Outline platelets.
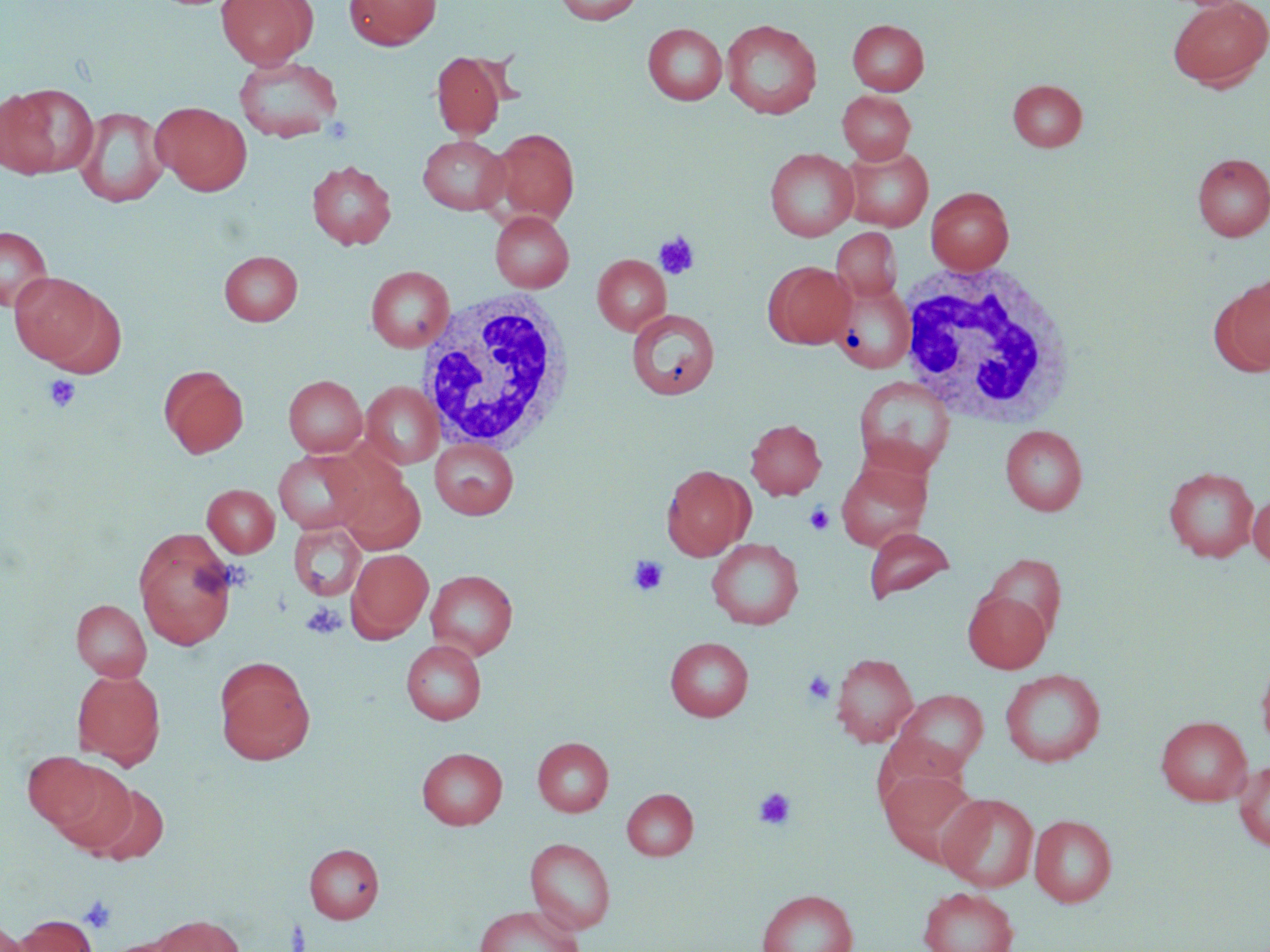

Approximate bounding boxes as [x1, y1, x2, y2] in pixels.
Platelets: [654, 231, 699, 280], [43, 374, 81, 412], [804, 503, 835, 535], [628, 555, 669, 596], [300, 602, 346, 639], [803, 671, 836, 705], [754, 787, 797, 830], [78, 894, 117, 933].

slide-level diagnosis = no evidence of blood parasites
magnification = 1000x
image size = 1270×952 pixels
stain = May-Grünwald-Giemsa
preparation = thin blood film
white blood cell locations = approximate bounding boxes as [x1, y1, x2, y2] in pixels: [894, 262, 1078, 428], [414, 288, 576, 454]
uninfected red blood cell locations = approximate bounding boxes as [x1, y1, x2, y2] in pixels: [216, 0, 318, 68], [344, 0, 442, 49], [554, 0, 643, 25], [1167, 0, 1270, 90], [721, 19, 822, 119], [847, 19, 929, 95], [643, 23, 728, 105], [431, 51, 507, 138], [233, 55, 344, 143], [1007, 79, 1087, 151], [1, 84, 97, 178], [837, 91, 915, 163], [150, 101, 252, 196], [74, 106, 169, 208], [488, 128, 579, 225], [418, 135, 509, 215], [840, 144, 933, 231], [764, 148, 859, 241], [1193, 152, 1270, 241], [307, 160, 397, 249], [926, 187, 1014, 274], [490, 210, 574, 292], [0, 226, 53, 312], [831, 227, 901, 302], [218, 250, 303, 326], [592, 254, 670, 335], [765, 261, 855, 349], [366, 265, 454, 352], [9, 272, 107, 366], [1213, 276, 1270, 375], [834, 282, 920, 375], [627, 308, 719, 400], [159, 365, 249, 458], [283, 375, 367, 457], [853, 375, 956, 478], [361, 381, 444, 469], [745, 419, 826, 500], [1001, 425, 1087, 515], [429, 438, 519, 518], [274, 448, 374, 535], [835, 457, 932, 551], [661, 464, 754, 561], [1163, 466, 1259, 562], [338, 471, 425, 555], [202, 484, 280, 557], [1248, 491, 1270, 567], [289, 523, 366, 601], [863, 527, 955, 604], [133, 529, 238, 650], [707, 538, 804, 629], [347, 548, 433, 641], [982, 553, 1067, 641], [426, 569, 518, 659], [963, 590, 1051, 673], [71, 599, 151, 682], [665, 637, 753, 721], [401, 640, 486, 724], [1256, 648, 1270, 754], [832, 653, 918, 747], [214, 657, 315, 765], [73, 669, 165, 768], [1000, 669, 1105, 767], [891, 688, 989, 776], [1155, 715, 1252, 805], [532, 737, 613, 816], [417, 747, 507, 828], [23, 749, 111, 833], [47, 759, 137, 853], [1233, 761, 1270, 851], [878, 767, 980, 862], [88, 783, 169, 864], [622, 788, 698, 860], [938, 792, 1039, 892], [1029, 814, 1117, 907], [525, 837, 616, 933], [304, 843, 384, 923], [918, 887, 1018, 952], [757, 889, 857, 952], [474, 905, 583, 952], [152, 914, 244, 952], [16, 915, 96, 952], [0, 921, 29, 952]
field of view = one of a larger specimen
modality = optical microscopy